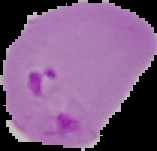
Summary:
  - Preparation: thin blood film
  - Result: Plasmodium parasites identified
  - Image type: cell region segmented out of the field of view; surrounding area masked to black
  - Image size: 157×151 pixels